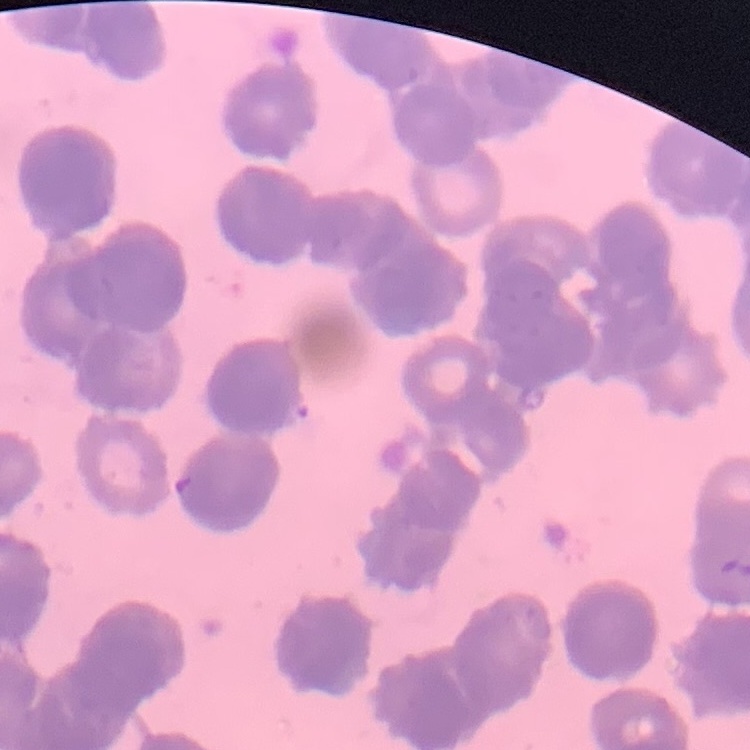 The red blood cells exhibit rouleaux formation. Field's or Giemsa stain. One tile cut from a larger photomicrograph. Thin blood smear.